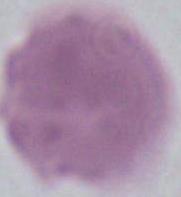
{
  "magnification": "1000x",
  "identification": "red blood cell",
  "modality": "micrograph"
}